Assess this cell for malaria.
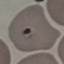

Parasitized.

Giemsa stain. Cell patch, automatically extracted from a larger field of view and resized to 64 × 64 pixels. Thin blood smear. Acquired by smartphone through the microscope eyepiece.